State the preparation type.
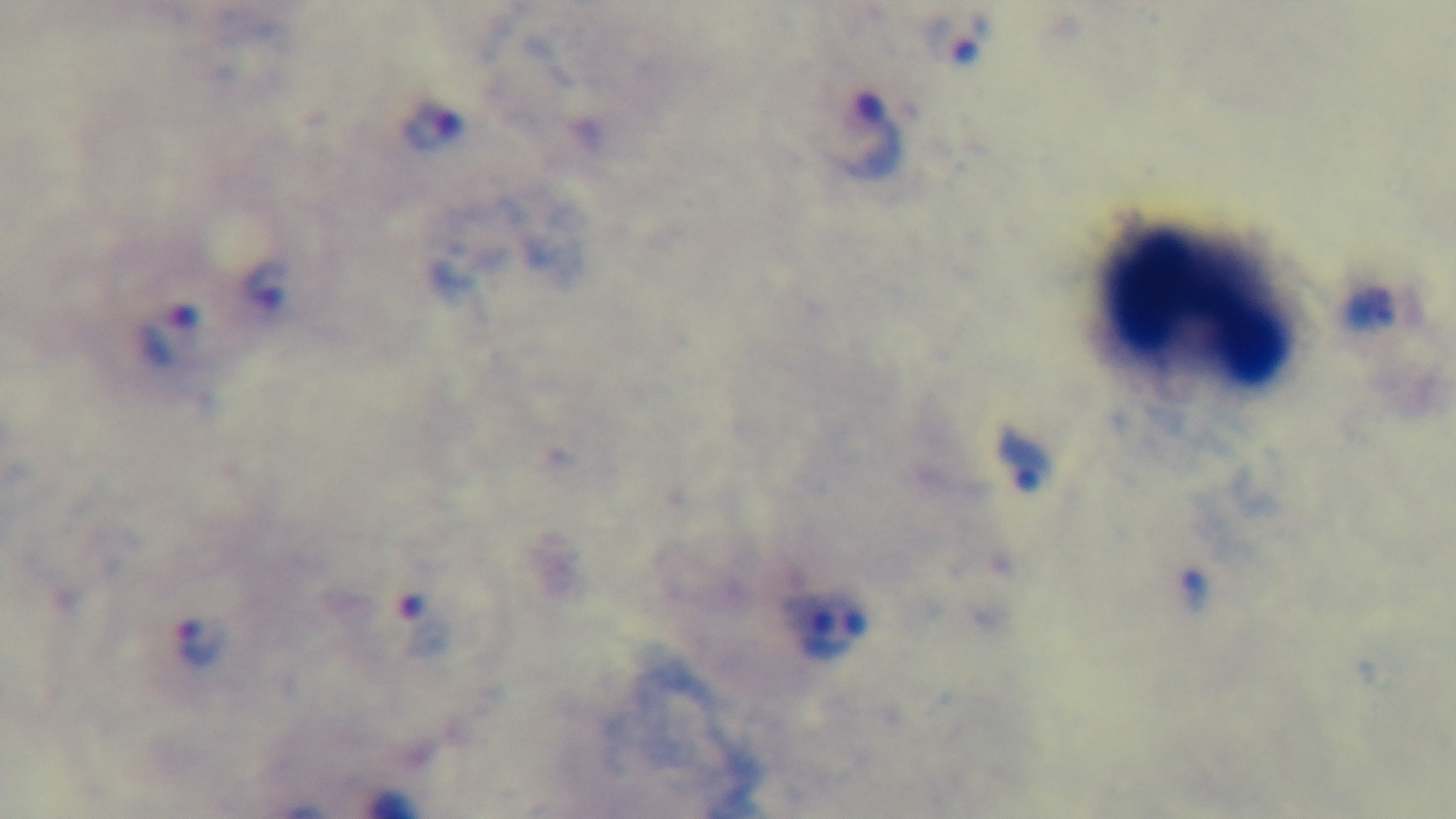
Thick.

field of view = one from the slide
stain = Giemsa
modality = light microscopy
malaria status = positive
capture = mounted 4K digital camera
objective = 100x oil immersion